Name the parasite shown.
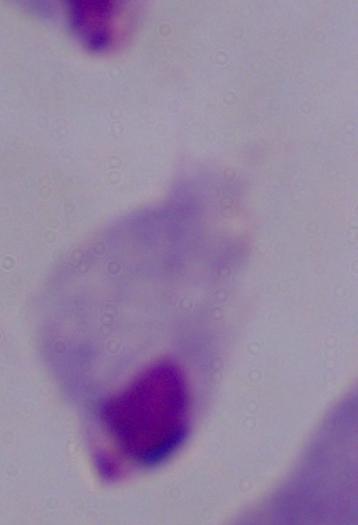
A trichomonad.

Micrograph. 1000x magnification.